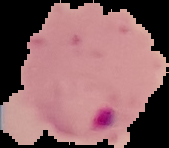 Segmented cell region on a black background. From a thin blood smear. Image is 169×148 pixels. Result: malaria parasites identified.